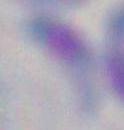

magnification = 1000x
identification = Toxoplasma gondii
modality = micrograph